Comment on the morphology of the erythrocytes.
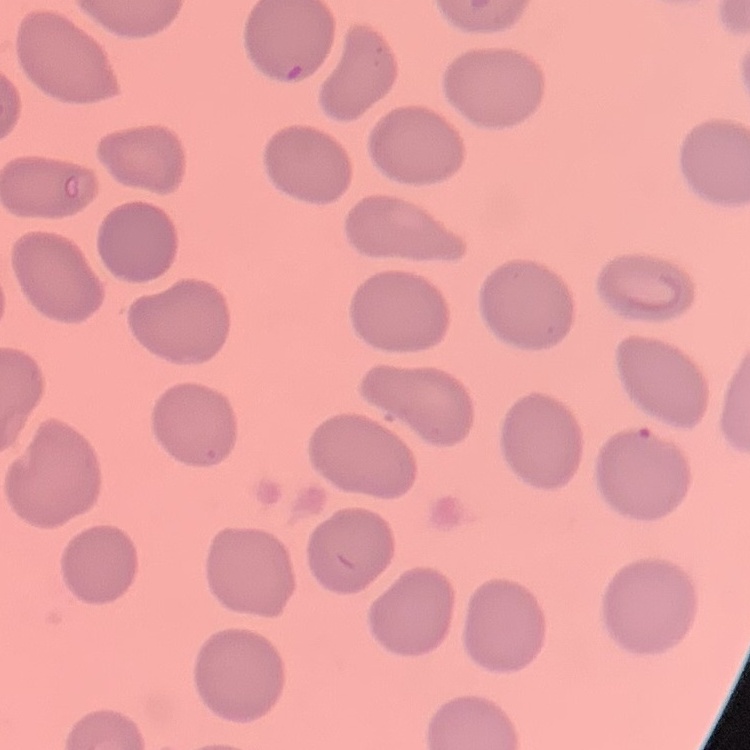

They show no rouleaux formation.

Thin blood smear. Stained with either Field's or Giemsa. One tile cut from a larger photomicrograph.